Assess this cell for malaria.
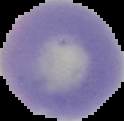

Uninfected.

Segmented cell region on a black background. Image is 124×121 pixels. From a thin blood smear.